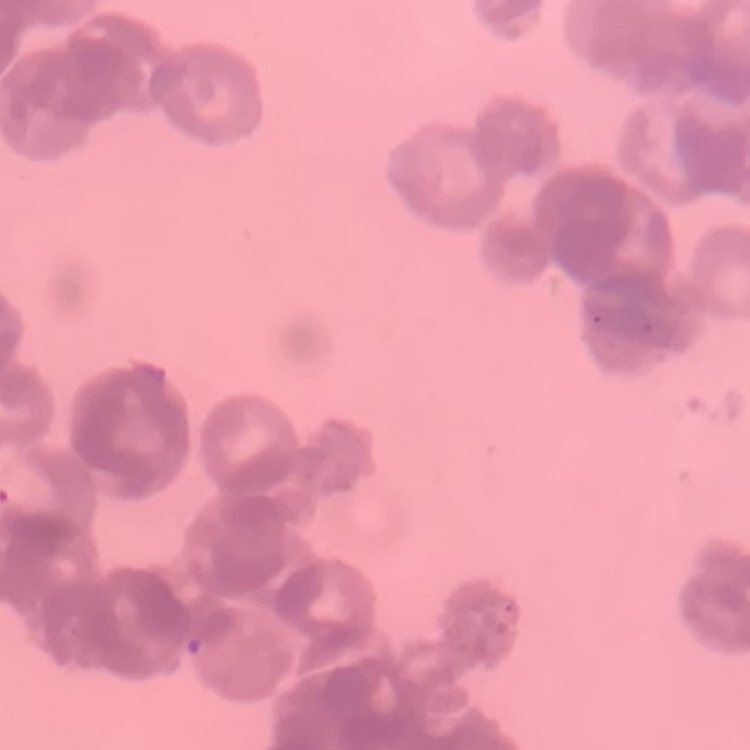

red blood cell morphology = rouleaux formation
image type = square crop of a larger photomicrograph
preparation = thin blood film
stain = Field's or Giemsa